Report the malaria status of this cell.
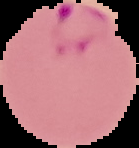

It is parasitized.

Image is 139×148 pixels. From a thin blood smear. Cell region segmented out of the field of view; the surrounding area is masked to black.